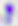

Summary:
  - Modality: micrograph
  - Magnification: 400x
  - Identification: Toxoplasma gondii